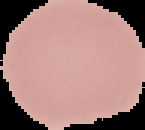

{
  "image_type": "cell region segmented out of the field of view; surrounding area masked to black",
  "preparation": "thin blood film",
  "image_size": "145×130 pixels",
  "result": "negative for malaria parasites"
}